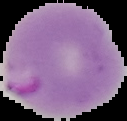 From a thin blood smear. Malaria status: parasitized. Segmented cell region on a black background. Image is 127×121 pixels.